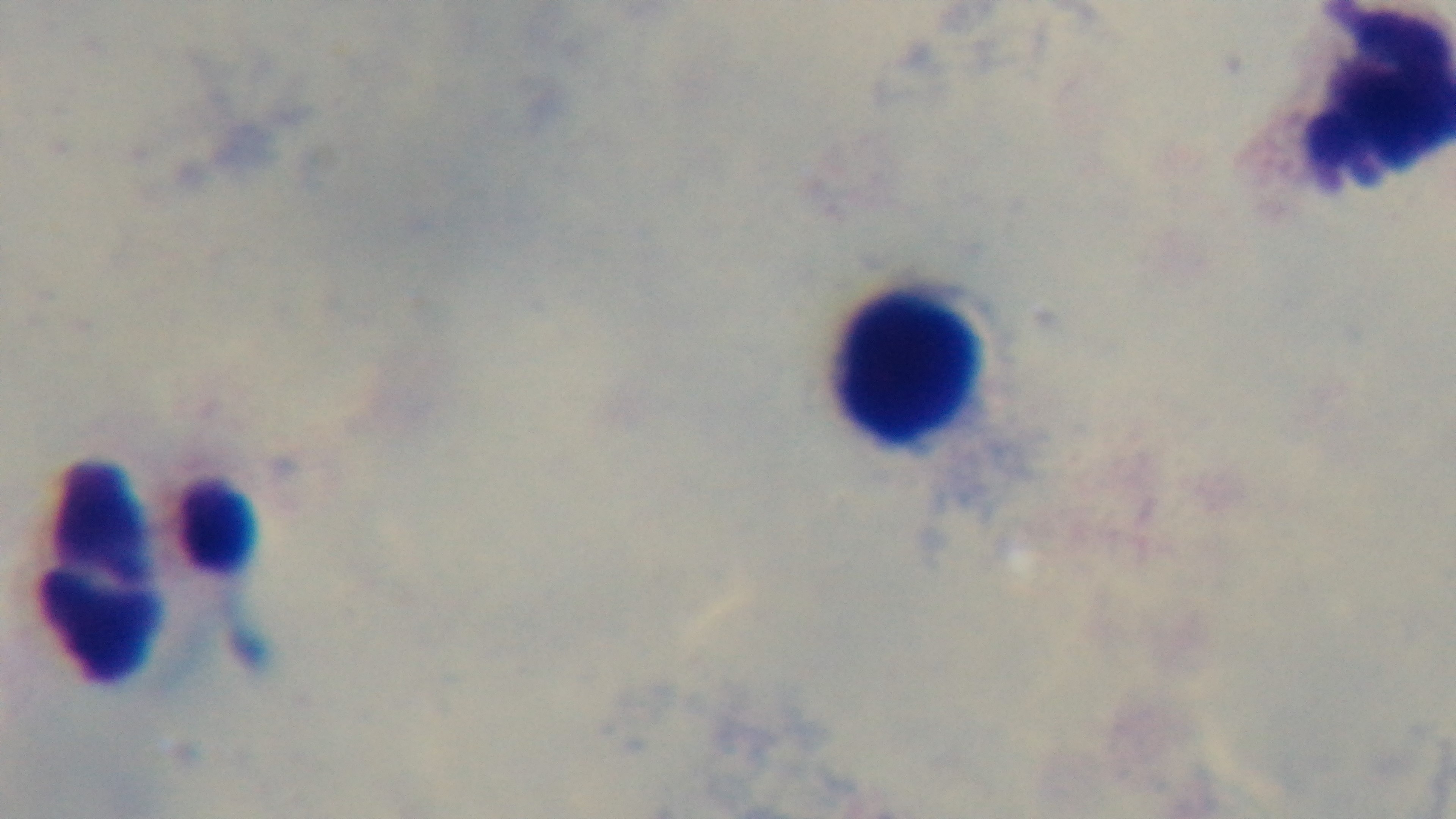
modality: light microscopy
preparation: thick blood film
capture: mounted 4K digital camera
malaria_status: uninfected
objective: 100x oil immersion
stain: Giemsa
field_of_view: single